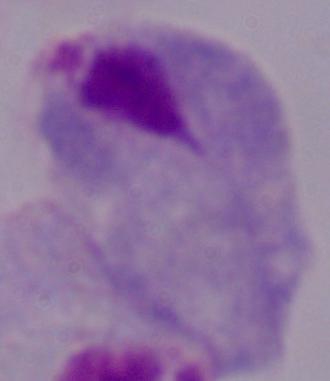

A trichomonad is shown. Captured at 1000x magnification. Micrograph.